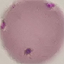
Result: negative for malaria parasites. Automatically extracted cell patch, resized to 64 × 64 pixels. Giemsa-stained preparation. Photographed with a smartphone camera at the microscope eyepiece. Thin blood film.